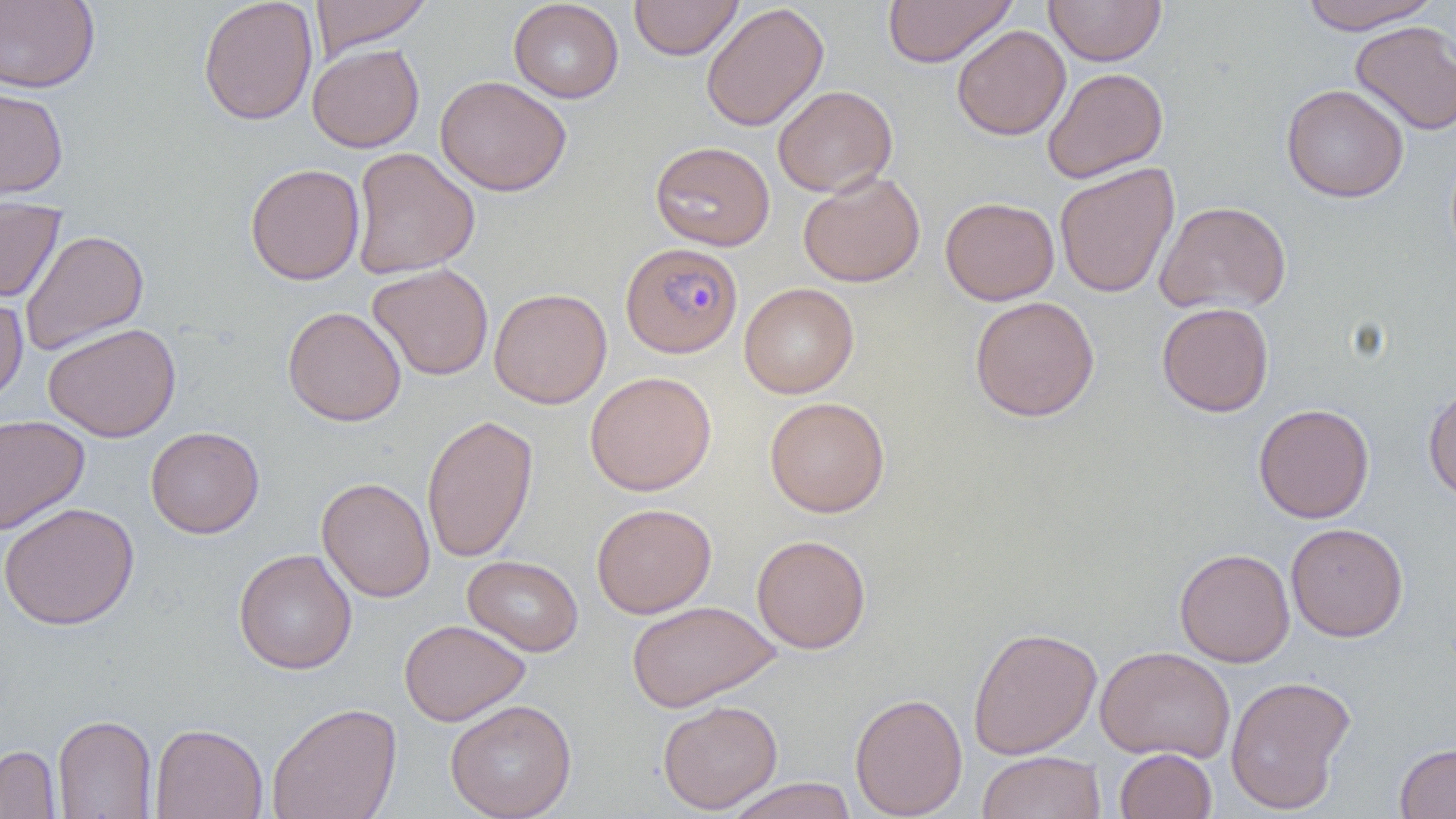

slide-level diagnosis = Plasmodium falciparum
field of view = single
magnification = 1000x
image size = 1456×819 pixels
preparation = thin blood smear
modality = light microscopy
uninfected red blood cell locations = approximate bounding boxes as (x1, y1, x2, y2) in pixels: (0, 0, 100, 94), (308, 0, 433, 57), (508, 0, 624, 103), (629, 0, 743, 60), (883, 0, 1016, 68), (1044, 0, 1166, 66), (1298, 0, 1442, 34), (198, 1, 318, 126), (700, 3, 829, 132), (1351, 20, 1456, 136), (951, 24, 1071, 140), (307, 43, 424, 153), (1042, 67, 1169, 183), (435, 75, 572, 197), (772, 84, 898, 197), (1280, 84, 1410, 203), (0, 87, 68, 200), (650, 141, 775, 251), (350, 147, 479, 279), (245, 163, 366, 285), (1054, 163, 1180, 298), (798, 171, 925, 287), (0, 197, 66, 303), (940, 197, 1060, 305), (1155, 199, 1292, 316), (19, 229, 149, 356), (368, 263, 494, 381), (739, 282, 858, 398), (0, 287, 28, 408), (488, 287, 612, 408), (969, 295, 1100, 421), (1156, 302, 1274, 417), (282, 306, 407, 427), (43, 322, 181, 442), (585, 371, 717, 496), (1423, 384, 1456, 503), (764, 396, 890, 517), (1253, 403, 1374, 524), (0, 413, 90, 535), (421, 413, 539, 563), (145, 426, 264, 538), (316, 476, 435, 602), (0, 502, 140, 631), (591, 502, 717, 619), (1286, 522, 1409, 642), (751, 533, 872, 654), (233, 548, 357, 674), (1174, 548, 1295, 668), (462, 554, 584, 657), (626, 600, 779, 712), (399, 619, 531, 726), (967, 625, 1102, 760), (1095, 646, 1235, 763), (1225, 675, 1356, 814), (850, 692, 968, 818), (445, 698, 577, 819), (658, 699, 783, 814), (266, 702, 402, 819), (52, 714, 157, 819), (149, 722, 268, 819), (1394, 742, 1456, 819), (0, 745, 62, 818), (1114, 748, 1218, 818), (976, 751, 1106, 819), (724, 777, 858, 819)